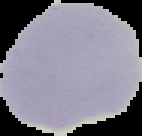

preparation = thin blood smear
image size = 142×136 pixels
result = no Plasmodium parasites seen
image type = segmented cell region on a black background